Classify this cell by malaria status.
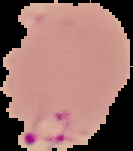
It is parasitized.

Cell region segmented out of the field of view; the surrounding area is masked to black. From a thin blood smear. Image is 133×151 pixels.